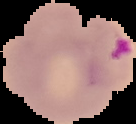

Image is 136×124 pixels. Result: malaria parasites identified. From a thin blood smear. Cell region segmented out of the field of view; the surrounding area is masked to black.